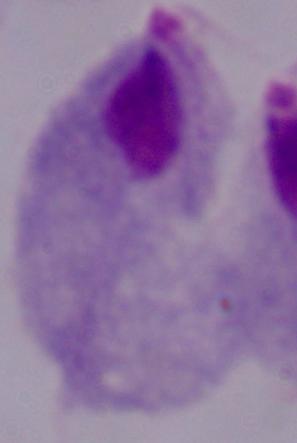
Summary:
  - Magnification: 1000x
  - Modality: micrograph
  - Identification: trichomonad